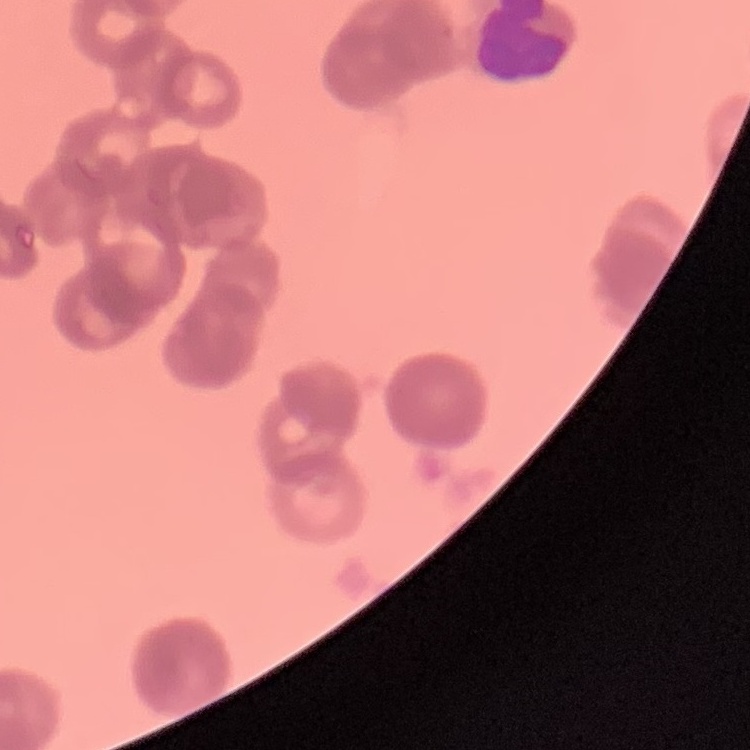 The erythrocytes exhibit rouleaux formation. Field's or Giemsa stain. Square crop of a larger photomicrograph. Thin peripheral smear.